Comment on the morphology of the erythrocytes.
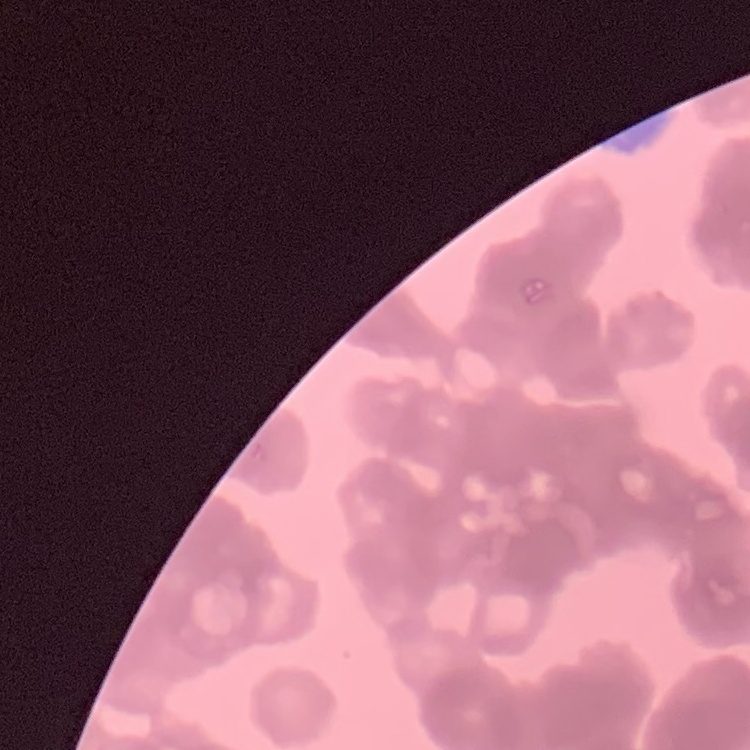
They show rouleaux formation.

image type = square crop of a larger photomicrograph
stain = Field's or Giemsa
preparation = thin blood film